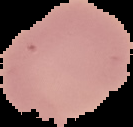
Summary:
  - Malaria status: uninfected
  - Image type: segmented cell region on a black background
  - Image size: 133×127 pixels
  - Preparation: thin blood smear